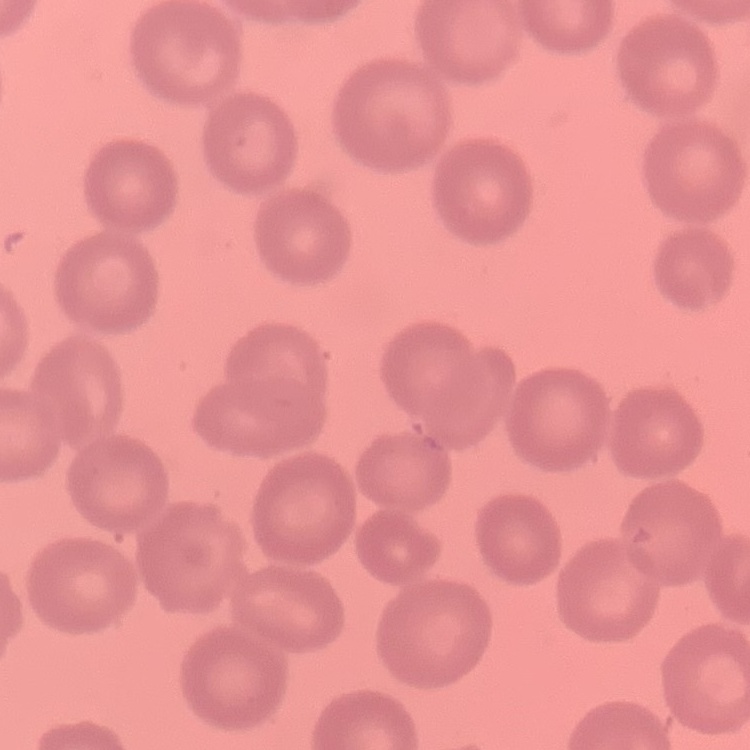

red blood cell morphology = no rouleaux formation
stain = Field's or Giemsa
image type = square crop of a larger photomicrograph
preparation = thin peripheral smear